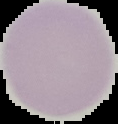
Image is 118×124 pixels. From a thin blood smear. Malaria status: uninfected. Segmented cell region on a black background.